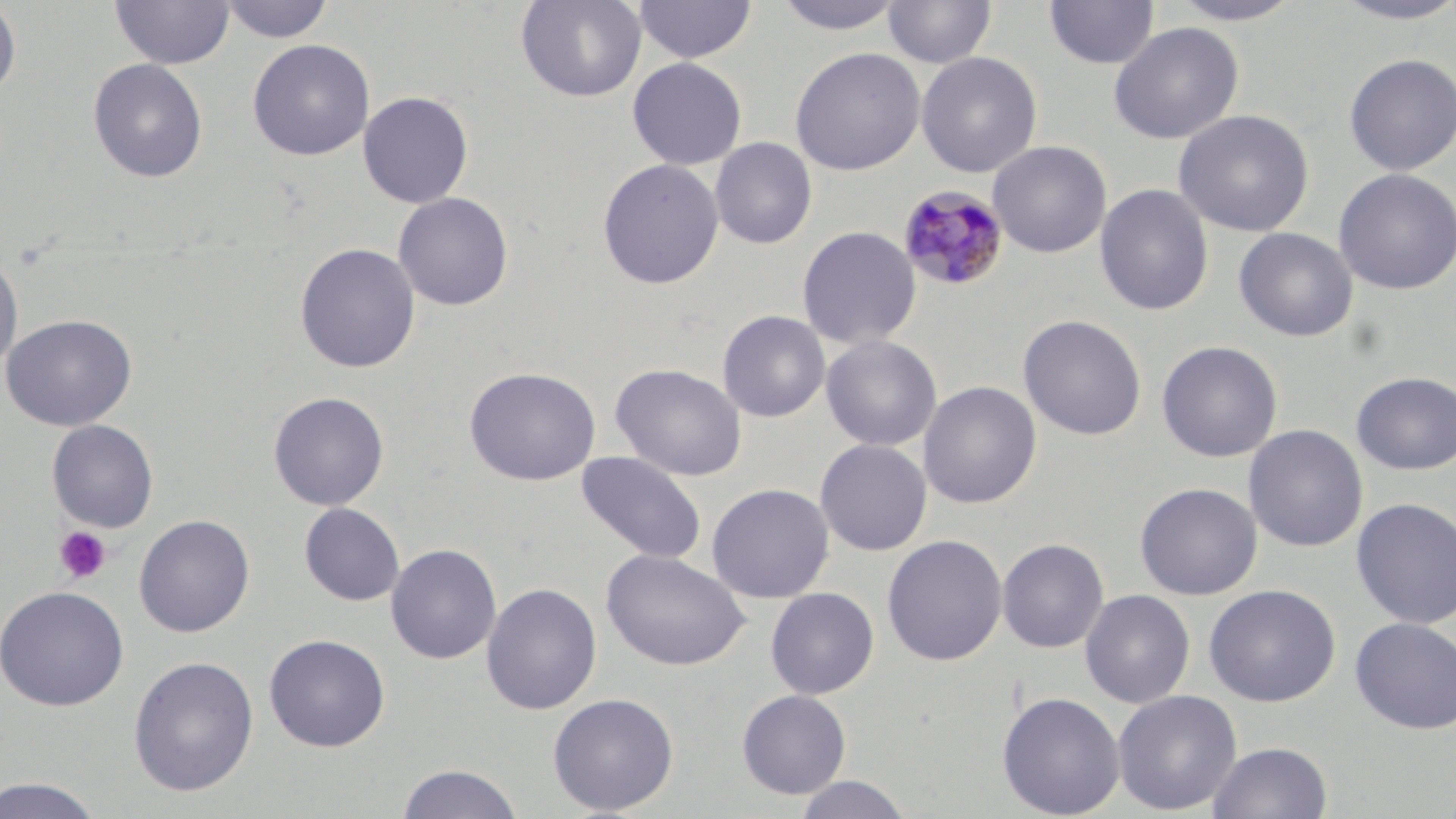

Summary:
  - Coordinate format: approximate bounding boxes as (x1, y1, x2, y2) in pixels
  - Uninfected red blood cell locations: (219, 0, 333, 43), (515, 0, 647, 102), (772, 0, 905, 35), (883, 0, 997, 68), (1044, 0, 1160, 69), (1164, 0, 1308, 26), (0, 1, 22, 102), (109, 1, 234, 70), (633, 1, 756, 63), (1330, 1, 1456, 26), (1108, 21, 1244, 144), (247, 39, 375, 160), (790, 46, 925, 176), (916, 52, 1042, 177), (1343, 53, 1456, 175), (627, 57, 747, 170), (87, 58, 208, 183), (358, 91, 473, 208), (1173, 109, 1314, 237), (710, 137, 817, 249), (987, 140, 1112, 258), (597, 158, 724, 290), (1333, 168, 1456, 295), (1095, 183, 1214, 316), (392, 191, 514, 311), (796, 226, 921, 349), (1233, 227, 1358, 342), (295, 242, 421, 373), (0, 253, 23, 379), (717, 310, 831, 422), (1, 314, 137, 432), (1018, 314, 1147, 440), (820, 334, 942, 451), (1156, 340, 1283, 462), (611, 362, 747, 481), (464, 366, 601, 486), (1351, 371, 1456, 475), (918, 381, 1041, 508), (268, 391, 389, 511), (46, 419, 158, 532), (1243, 424, 1368, 552), (815, 439, 932, 556), (576, 451, 707, 564), (1134, 481, 1263, 600), (706, 482, 835, 603), (1350, 496, 1456, 630), (299, 502, 404, 606), (134, 514, 254, 637), (882, 534, 1007, 666), (997, 538, 1109, 653), (386, 543, 501, 665), (600, 548, 749, 671), (481, 582, 602, 715), (1203, 584, 1341, 706), (0, 585, 129, 710), (765, 587, 879, 699), (1080, 589, 1195, 708), (1350, 616, 1456, 735), (264, 633, 390, 752), (127, 655, 259, 796), (736, 689, 852, 799), (1112, 689, 1242, 816), (996, 691, 1126, 818), (547, 692, 679, 815), (1207, 741, 1334, 819), (396, 763, 524, 819), (0, 774, 109, 818), (791, 774, 915, 818)
  - Plasmodium malariae-infected red blood cell locations: (897, 185, 1010, 291)
  - Platelet locations: (53, 525, 113, 585)
  - Slide-level diagnosis: Plasmodium malariae
  - Magnification: 1000x
  - Preparation: thin blood smear
  - Stain: May-Grünwald-Giemsa
  - Modality: optical microscopy
  - Field of view: single
  - Image size: 1456×819 pixels